Report the malaria status of this cell.
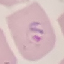
It is parasitized.

{
  "image_type": "automatically extracted cell patch, resized to 64 × 64 pixels",
  "capture": "smartphone through the microscope eyepiece",
  "stain": "Giemsa",
  "preparation": "thin blood film"
}